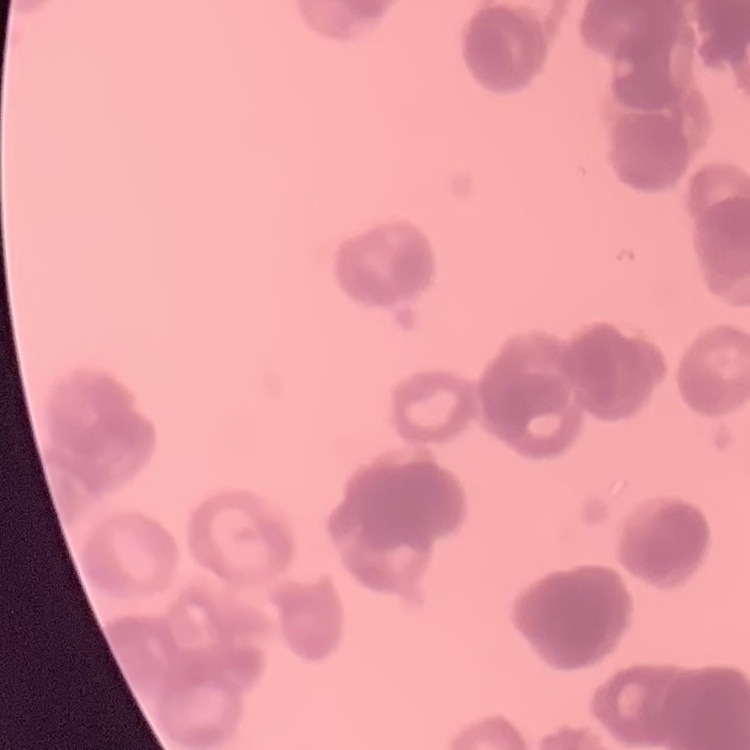

red blood cell morphology = rouleaux formation
stain = Field's or Giemsa
image type = one tile cut from a larger photomicrograph
preparation = thin peripheral smear